Give the extent of all Plasmodium parasites.
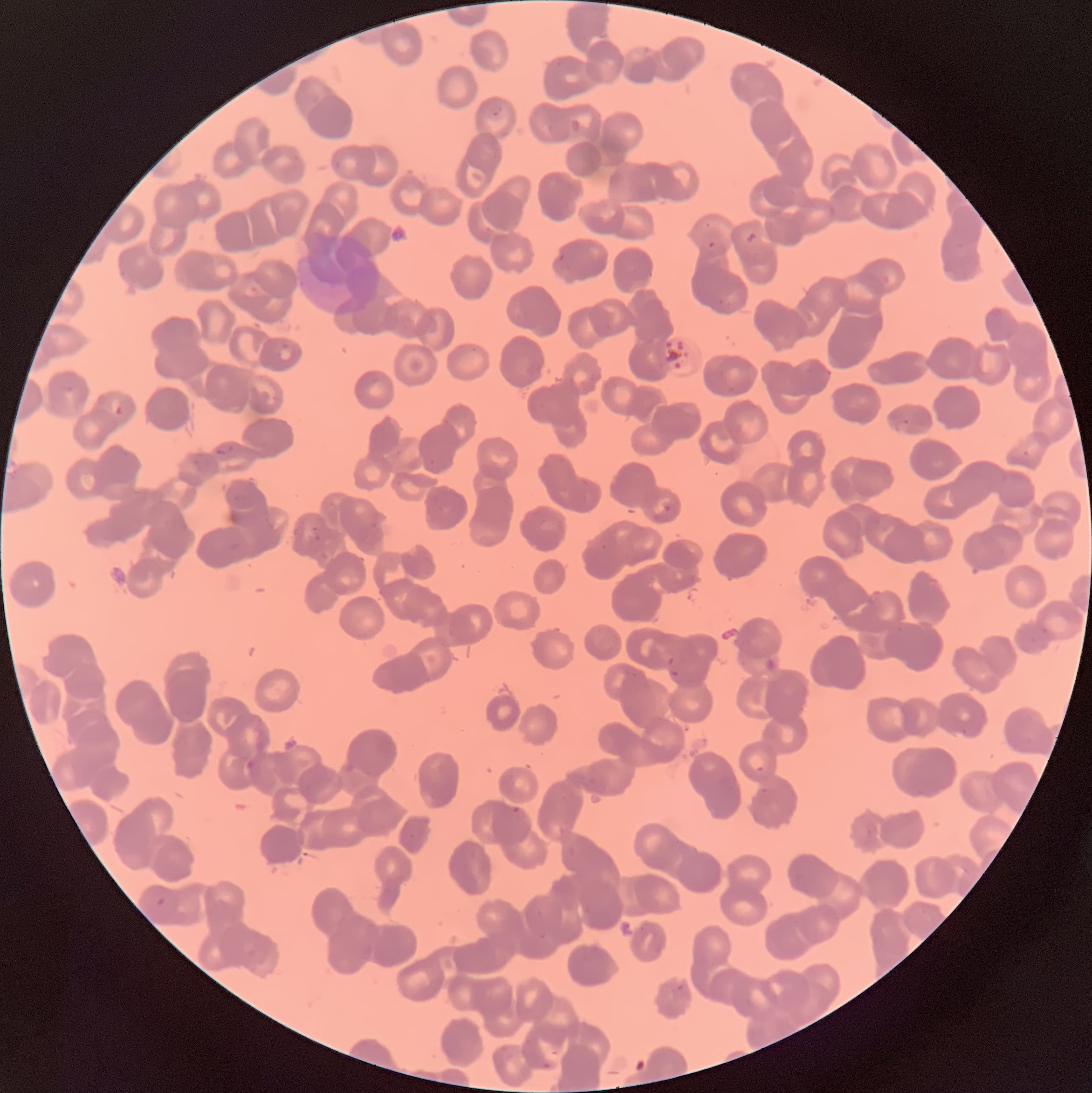
Approximate bounding boxes as (x1, y1, x2, y2) in pixels.
Plasmodium parasites: (491, 104, 504, 117), (745, 231, 757, 244), (707, 239, 716, 250), (113, 406, 124, 416), (216, 444, 235, 456), (660, 500, 675, 512), (310, 526, 322, 542), (665, 657, 682, 679), (755, 766, 765, 774), (511, 807, 522, 814), (154, 895, 167, 909), (676, 984, 685, 992), (541, 1061, 554, 1071).

{
  "red_blood_cell_morphology": "rouleaux formation",
  "preparation": "thin blood film",
  "modality": "optical microscopy",
  "image_size": "1092×1093 pixels"
}